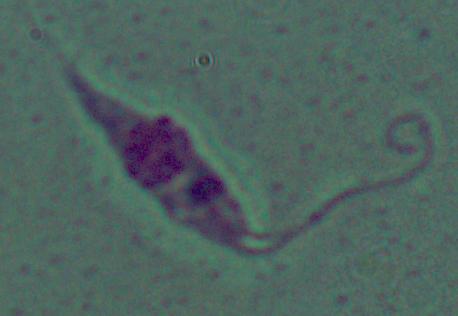
A Leishmania parasite is shown. Micrograph. 1000x magnification.